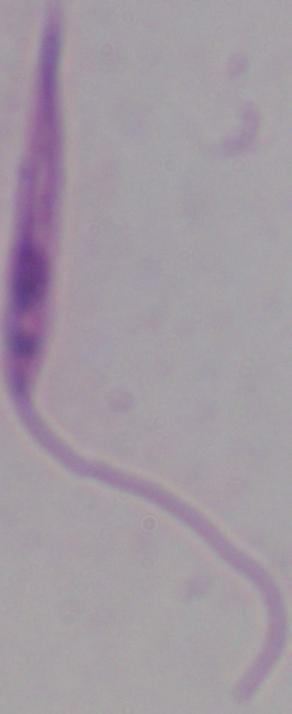

modality = micrograph
identification = Leishmania
magnification = 1000x